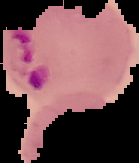 Cell region segmented out of the field of view; the surrounding area is masked to black. From a thin blood film. Malaria status: parasitized. Image is 139×163 pixels.